State the blood parasite species.
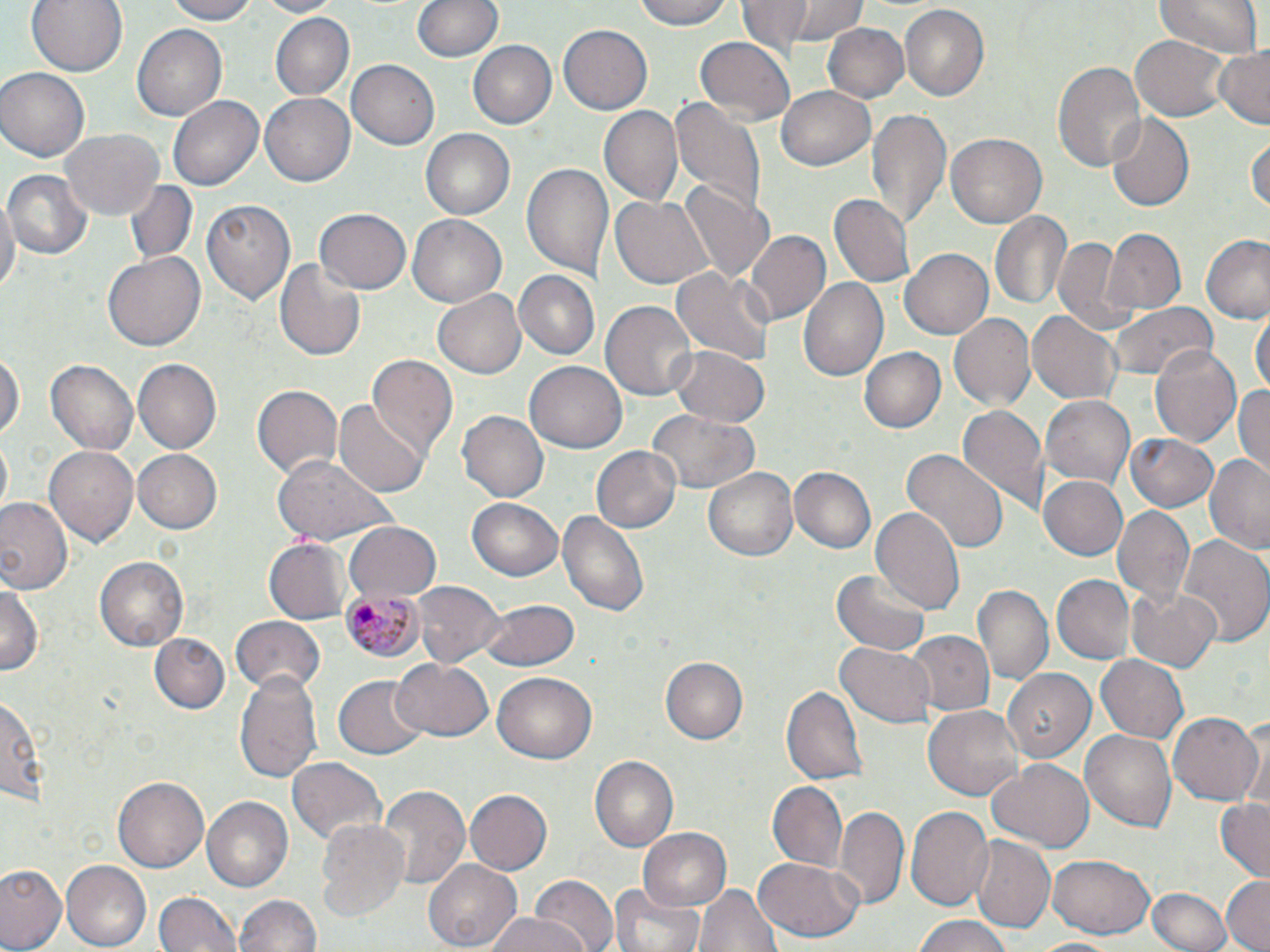

Plasmodium malariae.

Approximate bounding boxes as (x1,y1)-(x2,y2) corner pairs in pixels. Uninfected red blood cell locations: (27,0)-(129,78), (164,0)-(263,24), (255,0)-(340,15), (414,0)-(501,63), (633,0)-(734,31), (748,0)-(869,52), (1154,0)-(1261,59), (899,6)-(989,102), (270,12)-(352,101), (821,22)-(909,104), (558,24)-(652,115), (133,25)-(227,121), (1130,31)-(1230,119), (695,38)-(792,123), (469,41)-(556,129), (1213,46)-(1269,130), (1053,58)-(1146,172), (346,60)-(438,149), (0,67)-(89,162), (776,85)-(877,172), (167,92)-(262,189), (261,92)-(354,186), (668,96)-(768,216), (599,105)-(682,205), (868,106)-(951,228), (1106,114)-(1195,212), (420,127)-(515,217), (62,130)-(160,217), (1248,131)-(1270,215), (946,132)-(1047,229), (521,163)-(611,282), (2,167)-(92,261), (676,179)-(775,284), (121,182)-(201,269), (611,193)-(714,289), (830,194)-(912,285), (0,195)-(18,304), (199,195)-(294,305), (313,208)-(411,294), (991,211)-(1072,312), (407,214)-(507,308), (1105,228)-(1185,314), (743,229)-(830,327), (1053,234)-(1130,329), (1199,234)-(1270,323), (899,248)-(994,340), (103,252)-(205,352), (273,257)-(367,361), (670,265)-(774,367), (515,271)-(599,359), (800,277)-(890,384), (436,290)-(525,377), (602,299)-(698,402), (1107,302)-(1218,383), (1027,308)-(1122,406), (1252,310)-(1269,400), (947,312)-(1036,412), (671,344)-(770,427), (1149,345)-(1245,446), (0,346)-(23,445), (859,348)-(945,435), (367,357)-(459,457), (45,358)-(138,455), (135,358)-(222,453), (525,361)-(626,453), (1232,383)-(1270,476), (251,384)-(342,482), (1040,395)-(1134,486), (334,396)-(431,498), (960,406)-(1050,516), (647,408)-(760,494), (456,411)-(549,503), (1124,433)-(1222,513), (0,439)-(11,511), (42,443)-(139,548), (590,445)-(683,534), (133,449)-(223,532), (900,449)-(1009,555), (1204,453)-(1270,554), (270,456)-(395,547), (704,465)-(799,563), (788,466)-(875,553), (1038,475)-(1129,561), (467,496)-(564,581), (0,498)-(73,598), (1112,504)-(1194,610), (557,507)-(651,619), (870,507)-(965,614), (341,522)-(441,604), (1178,532)-(1270,647), (264,539)-(349,623), (96,557)-(189,650), (833,569)-(931,655), (1052,576)-(1134,661), (0,577)-(42,680), (412,580)-(505,667), (1125,582)-(1223,672), (975,584)-(1051,685), (483,598)-(580,672), (229,616)-(326,692), (902,629)-(995,716), (148,633)-(230,714), (836,639)-(934,727), (1094,653)-(1188,744), (391,657)-(492,742), (661,657)-(748,744), (1003,668)-(1097,762), (234,669)-(324,786), (492,672)-(598,763), (334,677)-(427,759), (781,683)-(870,786), (1,692)-(44,809), (922,704)-(1024,800), (1167,711)-(1262,807), (1081,730)-(1177,830), (589,756)-(680,852), (288,757)-(387,848), (988,761)-(1094,853), (110,776)-(209,873), (767,780)-(848,869), (375,785)-(469,893), (463,788)-(552,875), (200,796)-(293,893), (1215,797)-(1270,878), (835,804)-(908,910), (905,805)-(992,910), (315,817)-(410,922), (639,827)-(732,913), (969,837)-(1054,935), (1049,854)-(1153,938), (752,858)-(864,943), (59,861)-(149,950), (425,861)-(521,948), (0,864)-(66,952), (1220,875)-(1270,951), (530,878)-(619,952), (696,881)-(781,952), (611,886)-(703,952), (1147,887)-(1232,952), (152,890)-(243,952), (232,893)-(321,951), (485,914)-(585,952), (910,914)-(1016,952), (1026,936)-(1127,952). Plasmodium malariae-infected red blood cell locations: (343,586)-(422,663). One field of a larger specimen. Optical microscopy. Image is 1270×952 pixels. May-Grünwald-Giemsa stain. Captured at 1000x magnification. Thin blood film.